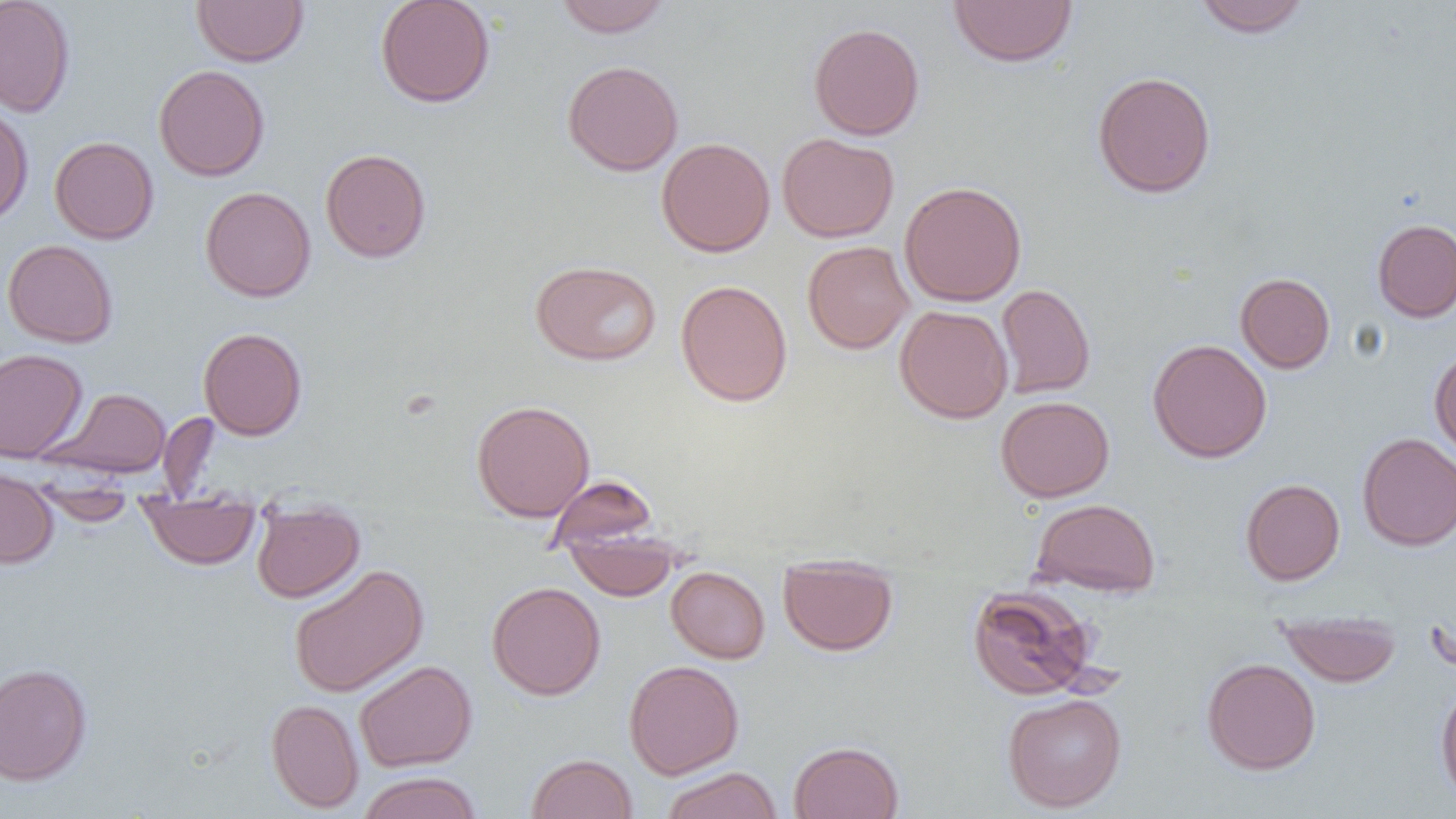
Approximate bounding boxes as (x1, y1, x2, y2) in pixels. Uninfected red blood cell locations: (0, 0, 75, 117), (192, 0, 308, 67), (375, 0, 495, 108), (555, 0, 671, 38), (948, 0, 1078, 68), (1193, 0, 1311, 38), (808, 22, 925, 140), (562, 60, 683, 176), (153, 64, 270, 181), (1092, 70, 1217, 198), (0, 104, 33, 227), (777, 132, 898, 242), (49, 136, 158, 244), (657, 137, 775, 257), (320, 148, 431, 263), (899, 180, 1027, 307), (200, 186, 316, 302), (1372, 218, 1456, 322), (2, 239, 118, 348), (802, 240, 913, 354), (530, 260, 662, 366), (1235, 272, 1335, 373), (676, 279, 793, 407), (996, 283, 1095, 398), (895, 304, 1013, 423), (198, 327, 307, 440), (1148, 339, 1272, 463), (0, 348, 87, 462), (1429, 348, 1456, 463), (44, 387, 172, 478), (996, 396, 1115, 502), (471, 399, 595, 522), (157, 412, 220, 502), (1357, 433, 1456, 551), (0, 467, 59, 569), (545, 475, 658, 554), (1240, 478, 1345, 585), (32, 487, 137, 526), (138, 491, 260, 569), (1031, 498, 1161, 597), (251, 501, 365, 603), (564, 529, 682, 600), (778, 554, 898, 656), (288, 564, 430, 697), (666, 566, 770, 663), (486, 581, 606, 700), (967, 584, 1099, 701), (1276, 610, 1402, 686), (1202, 658, 1321, 775), (354, 659, 477, 772), (624, 660, 744, 779), (0, 662, 92, 786), (1435, 680, 1456, 805), (1002, 692, 1126, 812), (266, 699, 364, 813), (788, 741, 904, 818), (526, 753, 638, 818), (660, 767, 783, 819), (357, 771, 482, 819). Slide-level diagnosis: no evidence of blood parasites. Thin blood smear. Captured at 1000x magnification. One field of a larger specimen. Image is 1456×819 pixels. Light microscopy.